Give the position of every Plasmodium parasite visible.
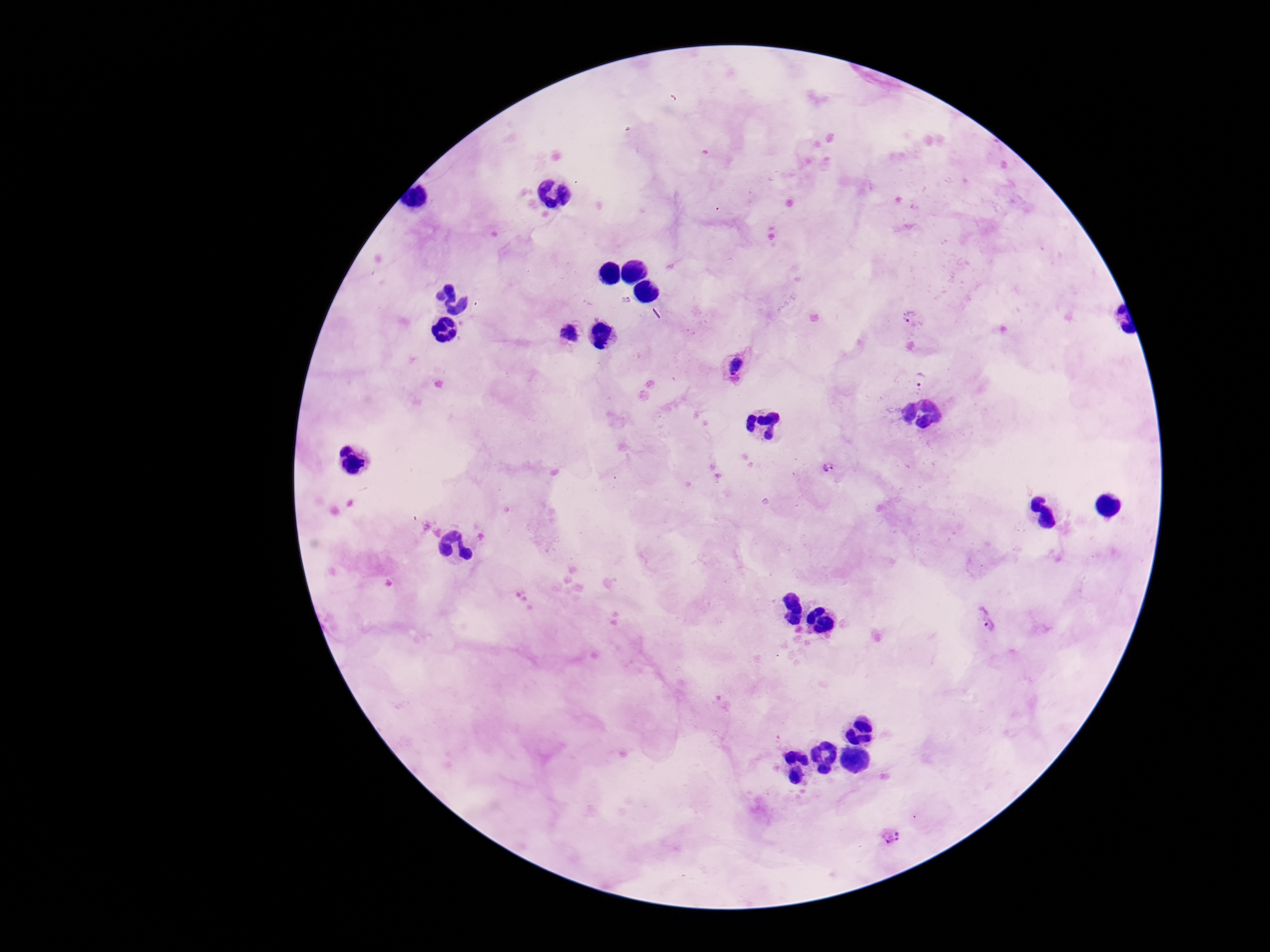
Approximate object centers, in pixels from the top-left corner.
Plasmodium parasites: (x=912, y=319), (x=570, y=336), (x=734, y=365), (x=918, y=379), (x=830, y=469), (x=987, y=619), (x=890, y=837).

Giemsa-stained preparation. Smartphone photograph taken through the microscope eyepiece. Thick blood smear. Image is 1270×952 pixels. Patient malaria status: infected. 100x magnification. One field from this slide.